Locate and identify every blood parasite.
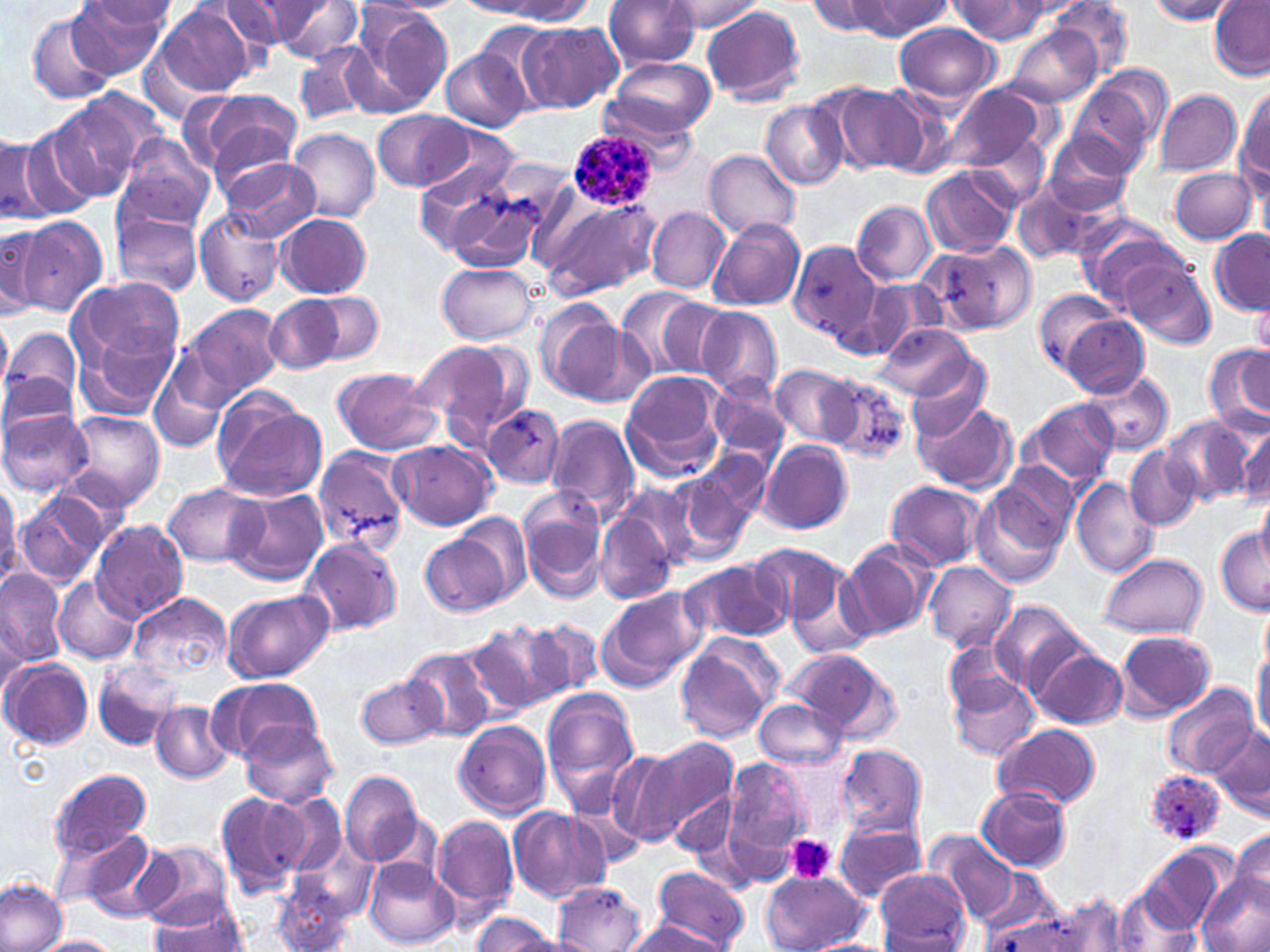
Approximate bounding boxes as named x1/y1/x2/y2 corners in pixels.
Plasmodium ovale-infected red blood cells: (x1=565, y1=128, x2=661, y2=211), (x1=1143, y1=768, x2=1226, y2=845).
No Plasmodium falciparum, Plasmodium malariae, Plasmodium vivax, Babesia divergens, or Trypanosoma brucei observed.

{
  "slide_level_diagnosis": "Plasmodium ovale",
  "modality": "optical microscopy",
  "platelet_locations": "approximate bounding boxes as named x1/y1/x2/y2 corners in pixels: (x1=787, y1=835, x2=835, y2=883)",
  "field_of_view": "single",
  "magnification": "1000x",
  "preparation": "thin blood smear",
  "stain": "May-Grünwald-Giemsa",
  "image_size": "1270×952 pixels",
  "uninfected_red_blood_cell_locations": "approximate bounding boxes as named x1/y1/x2/y2 corners in pixels: (x1=70, y1=0, x2=171, y2=79), (x1=604, y1=0, x2=701, y2=69), (x1=806, y1=0, x2=897, y2=36), (x1=1051, y1=0, x2=1135, y2=77), (x1=1145, y1=0, x2=1238, y2=24), (x1=1208, y1=0, x2=1270, y2=80), (x1=217, y1=1, x2=314, y2=51), (x1=262, y1=1, x2=363, y2=62), (x1=460, y1=1, x2=547, y2=16), (x1=662, y1=1, x2=763, y2=34), (x1=849, y1=1, x2=952, y2=39), (x1=950, y1=1, x2=1052, y2=43), (x1=87, y1=2, x2=180, y2=32), (x1=481, y1=2, x2=593, y2=22), (x1=155, y1=5, x2=254, y2=97), (x1=352, y1=5, x2=454, y2=112), (x1=702, y1=5, x2=804, y2=104), (x1=27, y1=11, x2=116, y2=104), (x1=517, y1=21, x2=622, y2=113), (x1=475, y1=22, x2=557, y2=100), (x1=894, y1=22, x2=999, y2=105), (x1=1005, y1=25, x2=1100, y2=106), (x1=294, y1=44, x2=379, y2=124), (x1=442, y1=51, x2=527, y2=131), (x1=607, y1=59, x2=716, y2=138), (x1=1091, y1=65, x2=1174, y2=147), (x1=829, y1=83, x2=929, y2=175), (x1=940, y1=83, x2=1046, y2=172), (x1=1237, y1=88, x2=1269, y2=184), (x1=1068, y1=89, x2=1151, y2=175), (x1=189, y1=90, x2=301, y2=182), (x1=1154, y1=90, x2=1242, y2=175), (x1=48, y1=96, x2=151, y2=200), (x1=761, y1=100, x2=848, y2=190), (x1=373, y1=110, x2=471, y2=188), (x1=22, y1=116, x2=118, y2=212), (x1=288, y1=127, x2=380, y2=223), (x1=966, y1=132, x2=1047, y2=212), (x1=1044, y1=133, x2=1138, y2=216), (x1=113, y1=134, x2=216, y2=232), (x1=3, y1=136, x2=44, y2=224), (x1=704, y1=149, x2=801, y2=239), (x1=215, y1=155, x2=321, y2=241), (x1=413, y1=157, x2=519, y2=246), (x1=921, y1=166, x2=1017, y2=259), (x1=1167, y1=167, x2=1258, y2=245), (x1=443, y1=177, x2=558, y2=275), (x1=1015, y1=181, x2=1113, y2=262), (x1=537, y1=196, x2=662, y2=297), (x1=852, y1=200, x2=937, y2=285), (x1=647, y1=207, x2=730, y2=293), (x1=193, y1=208, x2=287, y2=307), (x1=114, y1=213, x2=202, y2=297), (x1=275, y1=213, x2=373, y2=297), (x1=14, y1=215, x2=107, y2=317), (x1=708, y1=220, x2=805, y2=311), (x1=1079, y1=221, x2=1188, y2=309), (x1=1, y1=227, x2=43, y2=318), (x1=1208, y1=230, x2=1270, y2=316), (x1=934, y1=241, x2=1035, y2=334), (x1=791, y1=243, x2=891, y2=349), (x1=1120, y1=259, x2=1214, y2=349), (x1=437, y1=262, x2=539, y2=345), (x1=65, y1=276, x2=187, y2=378), (x1=863, y1=280, x2=947, y2=356), (x1=616, y1=286, x2=706, y2=377), (x1=1034, y1=288, x2=1124, y2=372), (x1=311, y1=291, x2=384, y2=364), (x1=266, y1=294, x2=345, y2=372), (x1=1250, y1=295, x2=1270, y2=361), (x1=534, y1=299, x2=629, y2=401), (x1=654, y1=299, x2=736, y2=376), (x1=175, y1=303, x2=286, y2=404), (x1=696, y1=306, x2=783, y2=400), (x1=1059, y1=312, x2=1150, y2=396), (x1=0, y1=317, x2=12, y2=394), (x1=71, y1=321, x2=180, y2=419), (x1=874, y1=324, x2=976, y2=400), (x1=3, y1=325, x2=83, y2=410), (x1=410, y1=339, x2=527, y2=440), (x1=1205, y1=344, x2=1270, y2=434), (x1=903, y1=355, x2=992, y2=441), (x1=149, y1=359, x2=227, y2=454), (x1=770, y1=364, x2=859, y2=446), (x1=330, y1=365, x2=442, y2=455), (x1=0, y1=370, x2=79, y2=437), (x1=622, y1=371, x2=730, y2=482), (x1=1081, y1=371, x2=1173, y2=456), (x1=825, y1=377, x2=912, y2=464), (x1=710, y1=379, x2=790, y2=462), (x1=213, y1=397, x2=326, y2=501), (x1=1020, y1=398, x2=1119, y2=490), (x1=914, y1=401, x2=1016, y2=494), (x1=482, y1=404, x2=565, y2=487), (x1=0, y1=408, x2=93, y2=497), (x1=63, y1=411, x2=165, y2=510), (x1=543, y1=413, x2=639, y2=522), (x1=1164, y1=416, x2=1252, y2=506), (x1=1233, y1=417, x2=1270, y2=507), (x1=389, y1=439, x2=497, y2=530), (x1=759, y1=439, x2=852, y2=533), (x1=309, y1=445, x2=411, y2=553), (x1=696, y1=446, x2=772, y2=534), (x1=1125, y1=446, x2=1200, y2=529), (x1=997, y1=462, x2=1079, y2=544), (x1=669, y1=470, x2=751, y2=559), (x1=0, y1=474, x2=21, y2=585), (x1=1070, y1=477, x2=1160, y2=578), (x1=885, y1=479, x2=984, y2=570), (x1=974, y1=479, x2=1071, y2=584), (x1=614, y1=481, x2=699, y2=577), (x1=163, y1=482, x2=264, y2=566), (x1=15, y1=487, x2=117, y2=585), (x1=223, y1=489, x2=330, y2=586), (x1=1256, y1=490, x2=1270, y2=576), (x1=519, y1=497, x2=606, y2=602), (x1=457, y1=512, x2=531, y2=602), (x1=595, y1=512, x2=675, y2=605), (x1=90, y1=520, x2=188, y2=621), (x1=1214, y1=524, x2=1270, y2=614), (x1=420, y1=531, x2=512, y2=619), (x1=300, y1=537, x2=403, y2=636), (x1=840, y1=539, x2=936, y2=640), (x1=746, y1=541, x2=846, y2=630), (x1=1097, y1=553, x2=1207, y2=639), (x1=683, y1=558, x2=792, y2=646), (x1=925, y1=561, x2=1016, y2=651), (x1=0, y1=568, x2=67, y2=667), (x1=785, y1=568, x2=877, y2=661), (x1=54, y1=576, x2=140, y2=665), (x1=221, y1=588, x2=332, y2=683), (x1=598, y1=588, x2=705, y2=689), (x1=128, y1=592, x2=232, y2=681), (x1=989, y1=600, x2=1086, y2=694), (x1=530, y1=619, x2=605, y2=699), (x1=465, y1=621, x2=564, y2=715), (x1=1116, y1=629, x2=1218, y2=720), (x1=675, y1=636, x2=780, y2=742), (x1=1253, y1=638, x2=1270, y2=744), (x1=942, y1=640, x2=1026, y2=722), (x1=1032, y1=646, x2=1127, y2=729), (x1=405, y1=647, x2=495, y2=741), (x1=788, y1=649, x2=901, y2=741), (x1=1, y1=658, x2=93, y2=749), (x1=93, y1=659, x2=184, y2=750), (x1=946, y1=668, x2=1040, y2=761), (x1=356, y1=674, x2=446, y2=750), (x1=207, y1=676, x2=321, y2=763), (x1=1164, y1=682, x2=1259, y2=779), (x1=542, y1=691, x2=639, y2=805), (x1=751, y1=697, x2=846, y2=769), (x1=151, y1=701, x2=236, y2=783), (x1=453, y1=720, x2=552, y2=817), (x1=240, y1=722, x2=340, y2=808), (x1=992, y1=723, x2=1102, y2=811), (x1=1209, y1=724, x2=1270, y2=821), (x1=639, y1=736, x2=737, y2=842), (x1=833, y1=744, x2=927, y2=839), (x1=605, y1=746, x2=690, y2=848), (x1=722, y1=756, x2=815, y2=865), (x1=47, y1=766, x2=151, y2=862), (x1=339, y1=769, x2=425, y2=868), (x1=978, y1=785, x2=1072, y2=871), (x1=216, y1=792, x2=309, y2=899), (x1=670, y1=792, x2=736, y2=857), (x1=274, y1=795, x2=345, y2=877), (x1=508, y1=807, x2=610, y2=903), (x1=431, y1=813, x2=518, y2=915), (x1=833, y1=819, x2=927, y2=902), (x1=56, y1=827, x2=169, y2=919), (x1=1227, y1=828, x2=1270, y2=909), (x1=929, y1=834, x2=1016, y2=924), (x1=135, y1=841, x2=232, y2=927), (x1=1140, y1=846, x2=1231, y2=935), (x1=365, y1=858, x2=457, y2=948), (x1=650, y1=866, x2=751, y2=950), (x1=874, y1=868, x2=969, y2=949), (x1=762, y1=871, x2=866, y2=950), (x1=1197, y1=876, x2=1269, y2=952), (x1=0, y1=878, x2=69, y2=952), (x1=553, y1=883, x2=646, y2=950), (x1=268, y1=884, x2=355, y2=951), (x1=1114, y1=888, x2=1193, y2=952), (x1=1055, y1=894, x2=1129, y2=951), (x1=147, y1=895, x2=248, y2=952), (x1=979, y1=909, x2=1078, y2=952), (x1=470, y1=913, x2=562, y2=951), (x1=623, y1=919, x2=732, y2=952), (x1=33, y1=935, x2=122, y2=952), (x1=803, y1=939, x2=895, y2=952)"
}